Locate and identify every blood parasite.
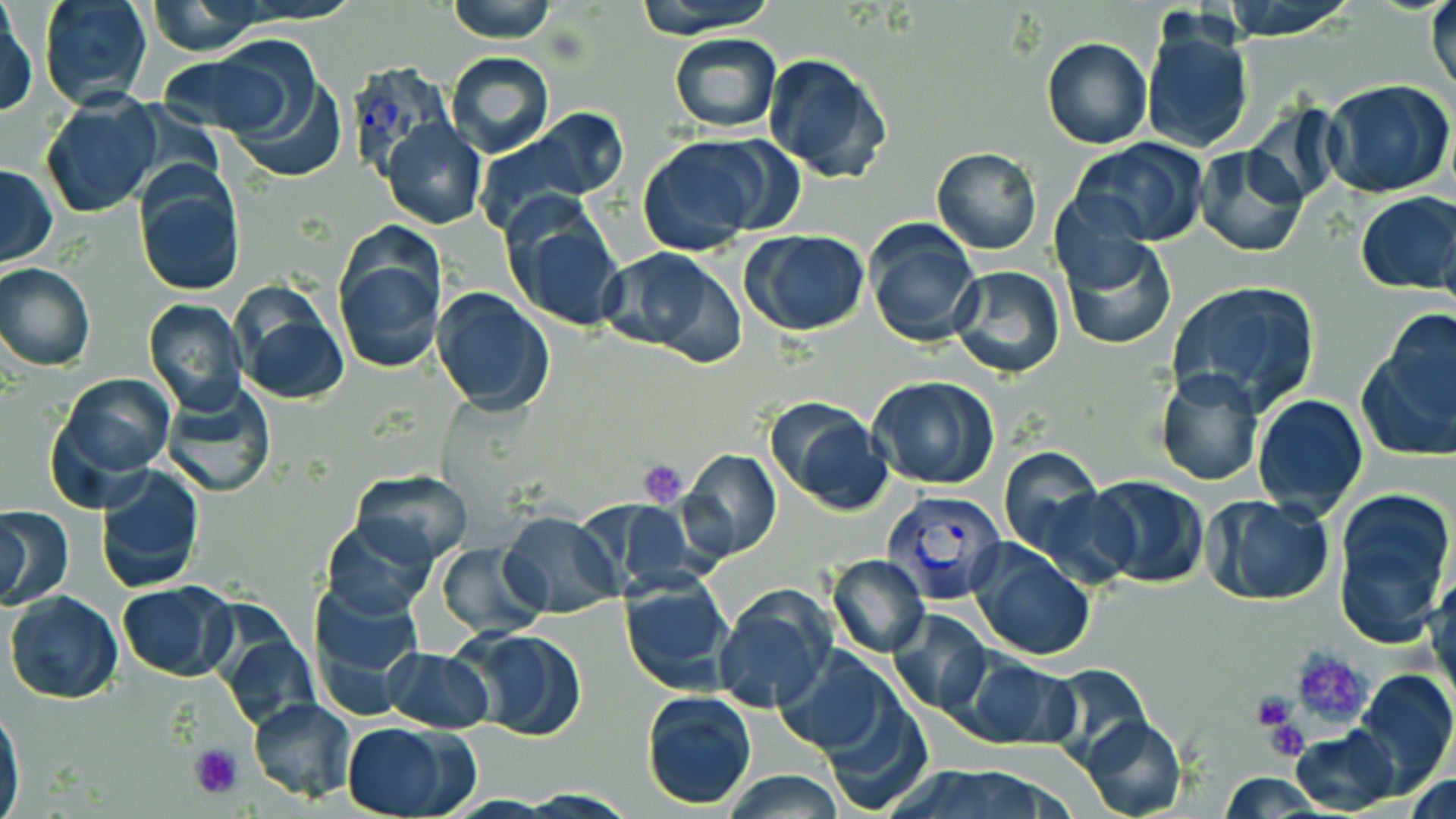

Approximate bounding boxes as named x1/y1/x2/y2 corners in pixels.
Plasmodium vivax-infected red blood cells: (x1=344, y1=62, x2=456, y2=179), (x1=885, y1=485, x2=1006, y2=609).
No Plasmodium falciparum, Plasmodium ovale, Plasmodium malariae, Babesia divergens, or Trypanosoma brucei observed.

Uninfected red blood cell locations: (x1=38, y1=0, x2=155, y2=111), (x1=444, y1=0, x2=561, y2=42), (x1=632, y1=0, x2=778, y2=36), (x1=1221, y1=0, x2=1359, y2=40), (x1=1427, y1=1, x2=1456, y2=100), (x1=143, y1=4, x2=267, y2=51), (x1=1, y1=8, x2=36, y2=120), (x1=1139, y1=23, x2=1254, y2=155), (x1=669, y1=34, x2=782, y2=132), (x1=1040, y1=37, x2=1153, y2=150), (x1=210, y1=41, x2=338, y2=159), (x1=162, y1=48, x2=305, y2=140), (x1=444, y1=52, x2=555, y2=157), (x1=762, y1=52, x2=893, y2=183), (x1=1324, y1=80, x2=1456, y2=198), (x1=41, y1=89, x2=163, y2=219), (x1=1242, y1=105, x2=1345, y2=208), (x1=483, y1=109, x2=628, y2=221), (x1=382, y1=119, x2=486, y2=230), (x1=635, y1=135, x2=774, y2=255), (x1=1070, y1=138, x2=1211, y2=247), (x1=1192, y1=144, x2=1310, y2=258), (x1=931, y1=146, x2=1042, y2=255), (x1=0, y1=163, x2=56, y2=267), (x1=134, y1=167, x2=247, y2=296), (x1=1354, y1=192, x2=1456, y2=294), (x1=1047, y1=193, x2=1153, y2=291), (x1=503, y1=202, x2=628, y2=330), (x1=1438, y1=209, x2=1456, y2=331), (x1=863, y1=220, x2=981, y2=347), (x1=331, y1=224, x2=447, y2=378), (x1=742, y1=230, x2=871, y2=337), (x1=1059, y1=236, x2=1177, y2=352), (x1=599, y1=246, x2=746, y2=365), (x1=0, y1=261, x2=95, y2=372), (x1=950, y1=265, x2=1066, y2=380), (x1=1166, y1=280, x2=1323, y2=414), (x1=229, y1=287, x2=349, y2=405), (x1=432, y1=288, x2=554, y2=415), (x1=142, y1=300, x2=248, y2=418), (x1=1359, y1=311, x2=1456, y2=461), (x1=1154, y1=367, x2=1264, y2=485), (x1=54, y1=373, x2=175, y2=481), (x1=869, y1=376, x2=1000, y2=489), (x1=158, y1=382, x2=278, y2=499), (x1=1251, y1=393, x2=1369, y2=519), (x1=764, y1=397, x2=894, y2=514), (x1=997, y1=446, x2=1104, y2=561), (x1=681, y1=449, x2=782, y2=561), (x1=94, y1=464, x2=205, y2=594), (x1=350, y1=470, x2=475, y2=564), (x1=1085, y1=475, x2=1211, y2=589), (x1=1332, y1=485, x2=1454, y2=641), (x1=1031, y1=488, x2=1140, y2=587), (x1=1202, y1=495, x2=1334, y2=606), (x1=577, y1=500, x2=698, y2=596), (x1=0, y1=505, x2=73, y2=611), (x1=1, y1=510, x2=34, y2=607), (x1=499, y1=512, x2=620, y2=619), (x1=321, y1=516, x2=439, y2=620), (x1=968, y1=538, x2=1096, y2=661), (x1=436, y1=543, x2=547, y2=638), (x1=827, y1=554, x2=930, y2=657), (x1=1427, y1=569, x2=1456, y2=710), (x1=618, y1=576, x2=736, y2=695), (x1=117, y1=580, x2=237, y2=680), (x1=309, y1=580, x2=425, y2=714), (x1=5, y1=591, x2=124, y2=705), (x1=711, y1=591, x2=836, y2=714), (x1=886, y1=609, x2=993, y2=716), (x1=211, y1=614, x2=321, y2=730), (x1=455, y1=627, x2=588, y2=742), (x1=382, y1=648, x2=495, y2=732), (x1=775, y1=648, x2=900, y2=757), (x1=949, y1=652, x2=1081, y2=752), (x1=1042, y1=663, x2=1154, y2=769), (x1=1354, y1=667, x2=1456, y2=792), (x1=814, y1=688, x2=934, y2=815), (x1=640, y1=689, x2=758, y2=809), (x1=246, y1=696, x2=357, y2=802), (x1=0, y1=704, x2=24, y2=814), (x1=1077, y1=715, x2=1188, y2=819), (x1=344, y1=721, x2=474, y2=819), (x1=1290, y1=729, x2=1397, y2=815), (x1=897, y1=767, x2=1067, y2=819), (x1=719, y1=770, x2=849, y2=818), (x1=1217, y1=772, x2=1326, y2=817), (x1=1408, y1=774, x2=1454, y2=819). Platelet locations: (x1=638, y1=461, x2=689, y2=507), (x1=1287, y1=649, x2=1372, y2=733), (x1=1250, y1=694, x2=1295, y2=730), (x1=1262, y1=718, x2=1311, y2=762), (x1=189, y1=742, x2=243, y2=799). Slide-level diagnosis: Plasmodium vivax. Thin blood smear. Light microscopy. 1000x magnification. One field of a larger specimen. May-Grünwald-Giemsa-stained preparation. Image is 1456×819 pixels.